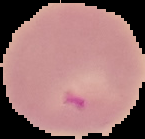
{
  "preparation": "thin blood film",
  "result": "malaria parasites detected",
  "image_type": "cell region segmented out of the field of view; surrounding area masked to black",
  "image_size": "145×139 pixels"
}